Classify the preparation.
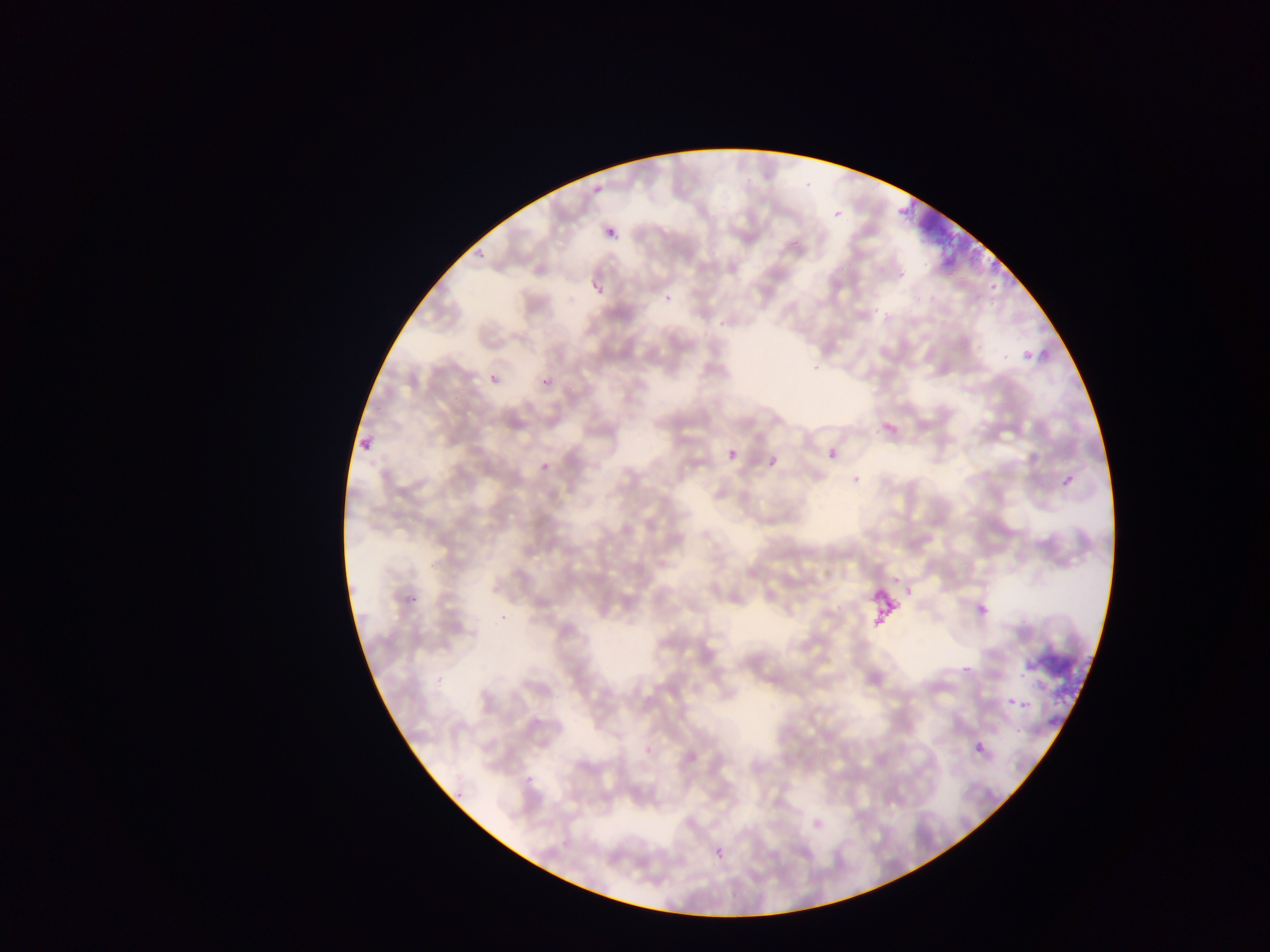

Thin blood smear.

Approximate bounding boxes as (left, top, right, bottom) in pixels. Plasmodium parasite locations: (829, 203, 846, 218), (598, 224, 622, 247), (470, 248, 488, 264), (581, 269, 614, 302), (989, 282, 1006, 300), (1019, 341, 1033, 369), (487, 368, 503, 385), (539, 368, 557, 391), (871, 423, 894, 439), (353, 427, 379, 451), (724, 436, 746, 460), (825, 439, 842, 464), (761, 451, 780, 462), (533, 456, 550, 473), (845, 468, 855, 484), (1056, 472, 1071, 491), (404, 581, 433, 604), (493, 586, 502, 596), (970, 589, 987, 608), (958, 655, 975, 677), (1011, 685, 1035, 718), (1001, 688, 1017, 705), (975, 742, 986, 752), (713, 848, 725, 864). Artifact (stain precipitate or debris) locations: (894, 198, 996, 270), (868, 588, 900, 622), (1029, 636, 1085, 699). Collected in Ghana. Photographed through a microscope with a mobile-phone camera. Single field of view. Image is 1270×952 pixels.